Assess this cell for malaria.
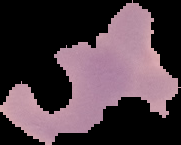
Uninfected.

image type = segmented cell region on a black background
image size = 181×145 pixels
preparation = thin blood film